Report the malaria status of this cell.
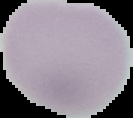
Uninfected.

Summary:
  - Preparation: thin blood film
  - Image type: segmented cell region on a black background
  - Image size: 133×118 pixels